Identify the blood parasite species.
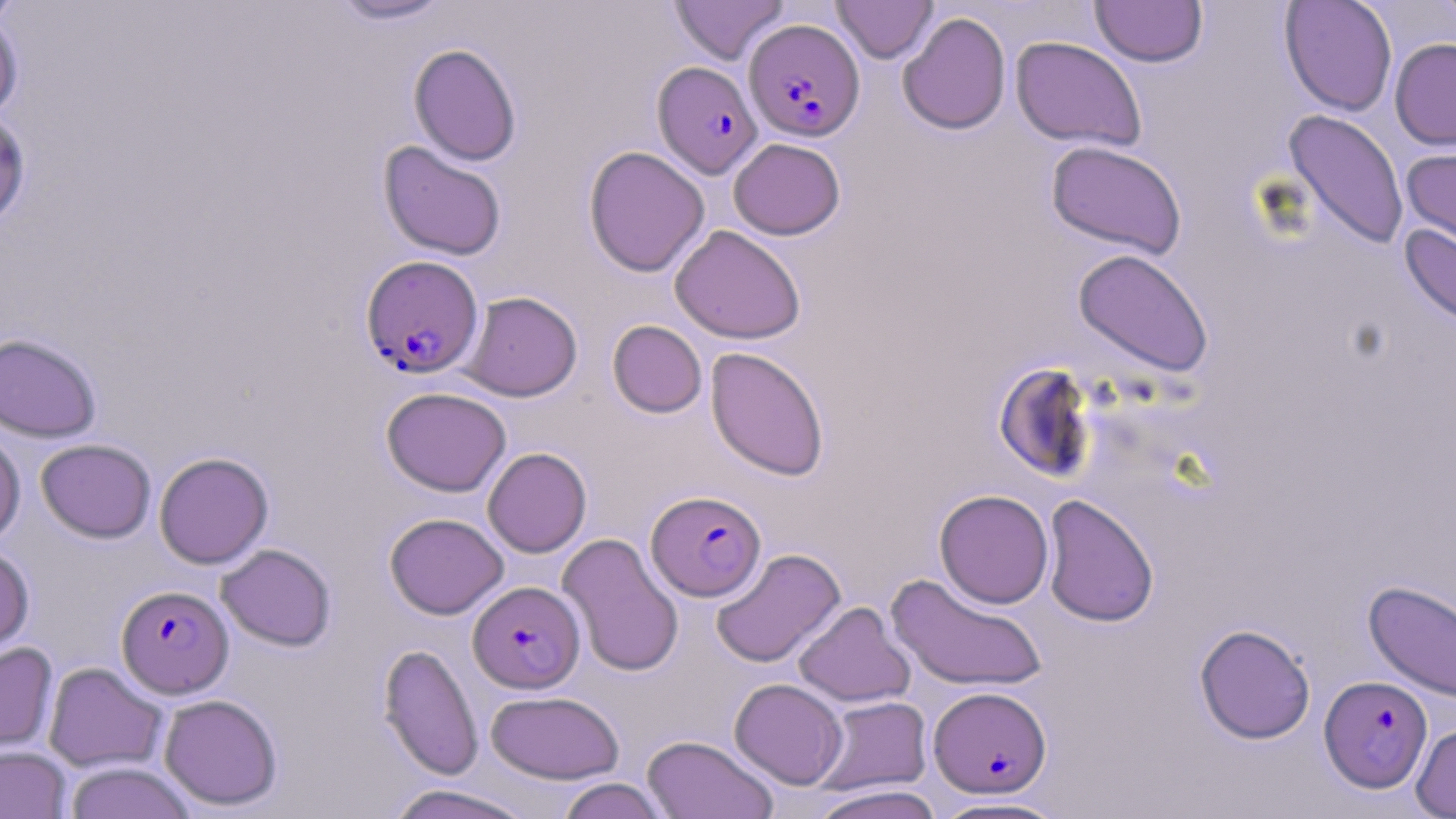

Plasmodium falciparum.

stain = May-Grünwald-Giemsa
modality = light microscopy
preparation = thin blood smear
image size = 1456×819 pixels
magnification = 1000x
field of view = one of a larger specimen
uninfected red blood cell locations = approximate bounding boxes as (x1, y1, x2, y2) in pixels: (0, 0, 22, 27), (328, 0, 454, 25), (668, 0, 789, 65), (1090, 0, 1209, 67), (1280, 0, 1397, 117), (1432, 0, 1456, 33), (831, 1, 938, 63), (0, 11, 24, 122), (897, 12, 1012, 135), (1010, 36, 1147, 152), (1390, 38, 1456, 150), (408, 43, 522, 166), (1283, 108, 1410, 250), (0, 109, 32, 229), (728, 138, 845, 240), (378, 141, 507, 260), (1046, 141, 1187, 259), (1400, 143, 1456, 253), (583, 145, 709, 277), (1400, 224, 1456, 328), (670, 225, 806, 344), (1073, 248, 1214, 378), (460, 291, 582, 401), (607, 320, 707, 418), (0, 332, 102, 442), (706, 347, 829, 481), (993, 362, 1096, 483), (381, 387, 511, 496), (0, 426, 25, 546), (36, 438, 156, 543), (483, 447, 592, 557), (154, 452, 273, 569), (934, 489, 1054, 608), (1041, 494, 1159, 628), (384, 513, 509, 619), (557, 532, 685, 677), (216, 543, 337, 651), (0, 544, 34, 658), (710, 547, 846, 668), (886, 573, 1048, 693), (1363, 580, 1456, 704), (793, 601, 915, 707), (1194, 624, 1316, 744), (0, 641, 58, 757), (378, 643, 484, 780), (43, 662, 167, 772), (730, 678, 848, 789), (485, 690, 624, 783), (158, 693, 283, 812), (813, 695, 933, 795), (1411, 721, 1456, 818), (642, 735, 779, 819), (0, 745, 71, 818), (64, 761, 197, 819), (555, 777, 672, 819), (384, 784, 537, 819), (807, 784, 946, 819), (930, 796, 1071, 818)
Plasmodium falciparum-infected red blood cell locations = approximate bounding boxes as (x1, y1, x2, y2) in pixels: (744, 19, 864, 141), (652, 61, 762, 178), (361, 255, 484, 379), (647, 490, 766, 601), (468, 581, 585, 693), (117, 585, 234, 698), (1319, 675, 1432, 793), (928, 686, 1052, 798)